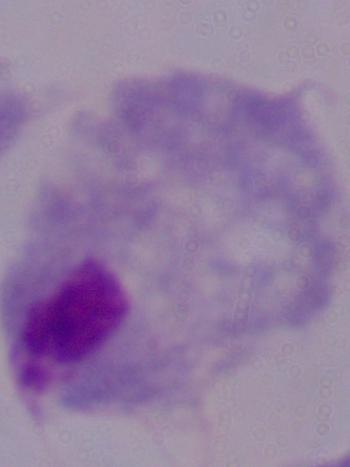

modality = micrograph
identification = trichomonad
magnification = 1000x